Identify the parasite.
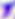
This is Toxoplasma gondii.

Summary:
  - Modality: photomicrograph
  - Magnification: 400x